Assess this cell for malaria.
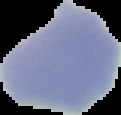
Uninfected.

Image is 121×115 pixels. From a thin blood smear. Cell region segmented out of the field of view; the surrounding area is masked to black.